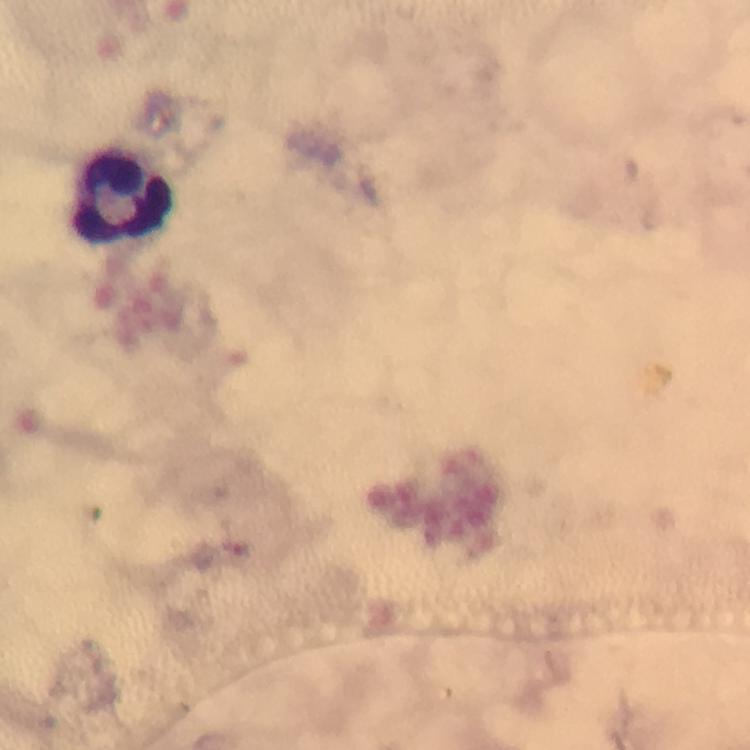
Approximate centers as (x, y) in pixels.
Summary:
  - Leukocyte locations: (125, 200)
  - Stain: Giemsa
  - Cropped from: one field of view
  - Malaria parasites: none detected
  - Capture: smartphone camera through the microscope
  - Preparation: thick blood smear
  - Magnification: 100x
  - Context: from a diagnostic examination for malaria
  - Image size: 750×750 pixels
  - Immersion oil: used